Point out every Plasmodium parasite.
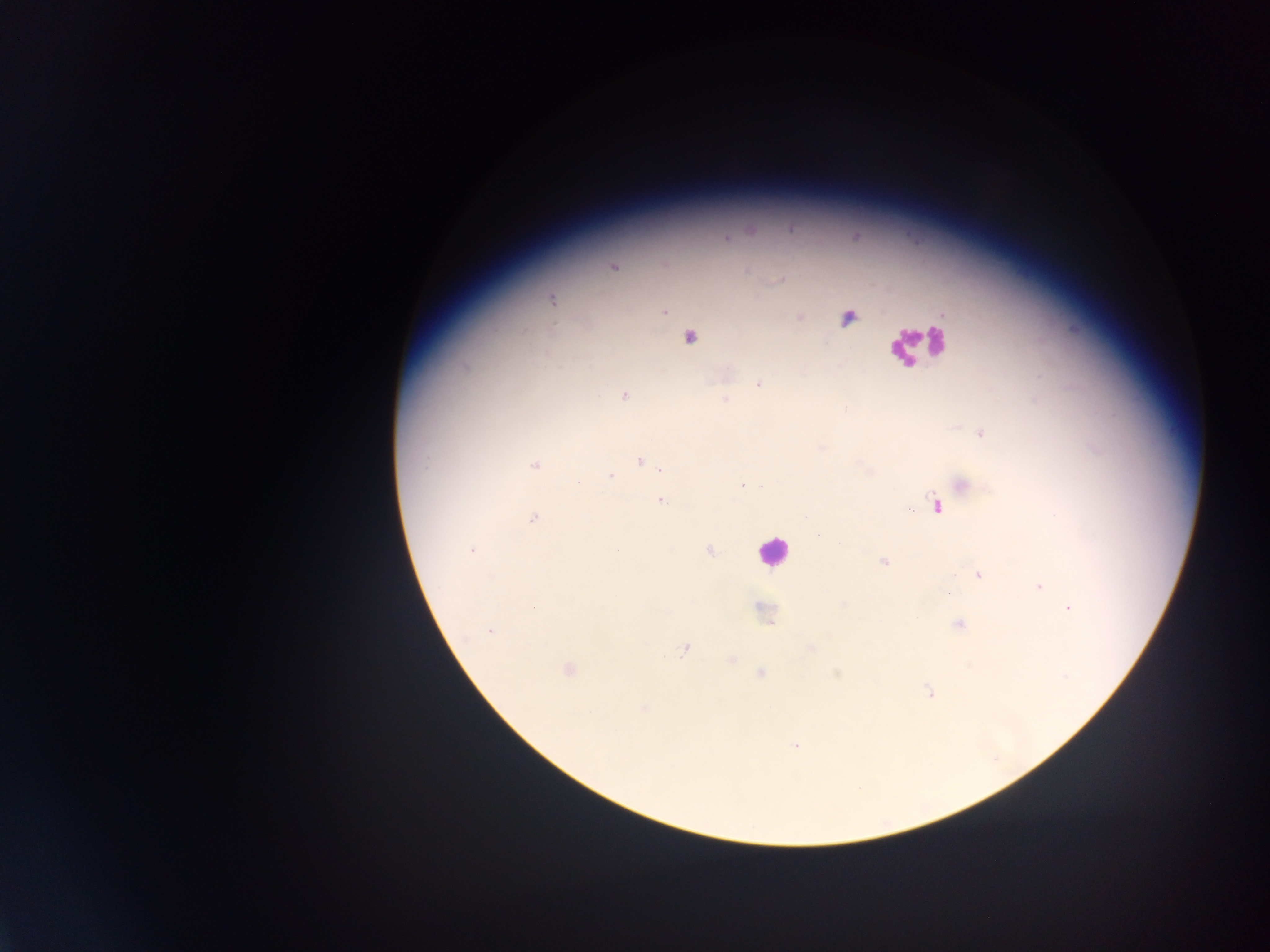
Approximate centers as x y in pixels.
Plasmodium parasites: 726 239; 614 267; 748 272; 779 280; 552 299; 665 311; 800 317; 848 317; 689 337; 465 367; 759 384; 624 396; 725 398; 981 433; 641 461; 535 465; 611 476; 578 483; 742 485; 963 485; 662 501; 936 505; 909 509; 805 516; 533 518; 472 549; 617 550; 709 551; 885 562; 978 575; 1039 587; 948 594; 843 604; 534 608; 1070 609; 958 625; 490 631; 812 649; 684 650; 732 659; 567 670; 761 674; 837 674; 1065 676; 929 693; 643 708; 796 746.

Summary:
  - Leukocyte locations: 917 343; 772 552
  - Preparation: thick blood film
  - Image size: 1270×952 pixels
  - Field of view: single
  - Country: Ghana
  - Capture: mobile-phone photograph through a microscope